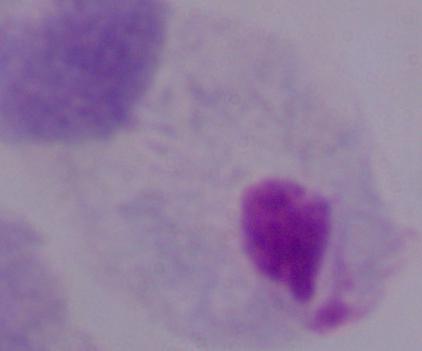

modality = photomicrograph
identification = trichomonad
magnification = 1000x